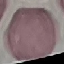

malaria status = uninfected
stain = Giemsa
image type = cell patch, automatically extracted from a larger field of view and resized to 64 × 64 pixels
capture = smartphone through the microscope eyepiece
preparation = thin blood smear